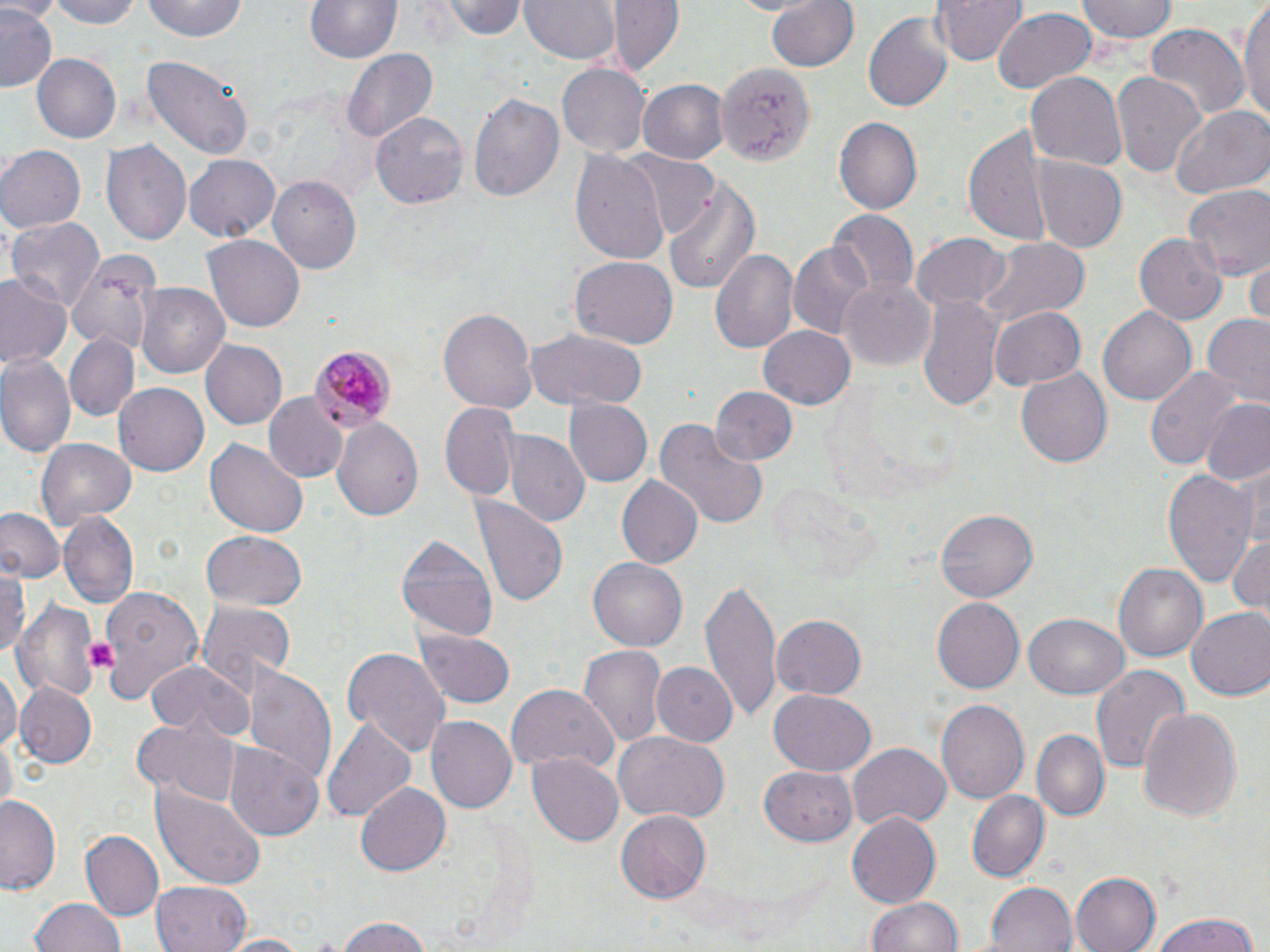
Summary:
  - Coordinate format: approximate bounding boxes as named x1/y1/x2/y2 corners in pixels
  - Platelet locations: (x1=85, y1=635, x2=118, y2=674)
  - Plasmodium malariae-infected red blood cell locations: (x1=310, y1=348, x2=396, y2=430)
  - Uninfected red blood cell locations: (x1=39, y1=0, x2=147, y2=28), (x1=140, y1=0, x2=250, y2=44), (x1=302, y1=0, x2=406, y2=65), (x1=442, y1=0, x2=527, y2=41), (x1=518, y1=0, x2=621, y2=63), (x1=608, y1=0, x2=684, y2=76), (x1=766, y1=0, x2=860, y2=75), (x1=930, y1=0, x2=1026, y2=65), (x1=1077, y1=0, x2=1178, y2=44), (x1=1239, y1=0, x2=1270, y2=123), (x1=0, y1=6, x2=60, y2=93), (x1=991, y1=6, x2=1095, y2=94), (x1=863, y1=11, x2=954, y2=112), (x1=1144, y1=26, x2=1250, y2=126), (x1=344, y1=50, x2=437, y2=144), (x1=142, y1=53, x2=253, y2=163), (x1=32, y1=55, x2=121, y2=144), (x1=715, y1=61, x2=814, y2=167), (x1=558, y1=65, x2=649, y2=155), (x1=1110, y1=69, x2=1206, y2=181), (x1=1025, y1=71, x2=1129, y2=171), (x1=640, y1=80, x2=728, y2=165), (x1=466, y1=92, x2=564, y2=204), (x1=1168, y1=104, x2=1270, y2=201), (x1=371, y1=112, x2=468, y2=211), (x1=835, y1=117, x2=922, y2=213), (x1=963, y1=123, x2=1053, y2=250), (x1=102, y1=139, x2=192, y2=245), (x1=0, y1=145, x2=84, y2=233), (x1=570, y1=151, x2=669, y2=261), (x1=625, y1=153, x2=722, y2=241), (x1=184, y1=155, x2=279, y2=241), (x1=1033, y1=157, x2=1126, y2=251), (x1=266, y1=172, x2=363, y2=274), (x1=663, y1=179, x2=759, y2=295), (x1=1185, y1=185, x2=1270, y2=281), (x1=1156, y1=202, x2=1264, y2=318), (x1=828, y1=209, x2=920, y2=297), (x1=7, y1=216, x2=103, y2=313), (x1=912, y1=233, x2=1010, y2=314), (x1=1135, y1=233, x2=1226, y2=326), (x1=202, y1=234, x2=305, y2=333), (x1=976, y1=237, x2=1092, y2=330), (x1=788, y1=243, x2=875, y2=341), (x1=64, y1=248, x2=156, y2=367), (x1=709, y1=248, x2=799, y2=355), (x1=570, y1=255, x2=677, y2=345), (x1=1247, y1=259, x2=1270, y2=325), (x1=0, y1=275, x2=69, y2=374), (x1=838, y1=278, x2=936, y2=369), (x1=135, y1=283, x2=230, y2=379), (x1=918, y1=289, x2=1001, y2=410), (x1=991, y1=304, x2=1086, y2=390), (x1=439, y1=305, x2=536, y2=417), (x1=1099, y1=306, x2=1196, y2=406), (x1=1202, y1=315, x2=1270, y2=407), (x1=757, y1=324, x2=856, y2=410), (x1=525, y1=329, x2=646, y2=410), (x1=63, y1=334, x2=140, y2=422), (x1=199, y1=339, x2=289, y2=431), (x1=0, y1=353, x2=76, y2=460), (x1=1018, y1=365, x2=1115, y2=468), (x1=1147, y1=365, x2=1242, y2=472), (x1=114, y1=384, x2=208, y2=475), (x1=709, y1=387, x2=797, y2=468), (x1=264, y1=393, x2=349, y2=484), (x1=565, y1=398, x2=652, y2=488), (x1=1199, y1=398, x2=1270, y2=485), (x1=441, y1=402, x2=519, y2=503), (x1=444, y1=414, x2=584, y2=512), (x1=331, y1=419, x2=424, y2=523), (x1=654, y1=419, x2=768, y2=531), (x1=504, y1=432, x2=590, y2=528), (x1=37, y1=439, x2=135, y2=527), (x1=204, y1=439, x2=309, y2=539), (x1=1236, y1=467, x2=1269, y2=555), (x1=1161, y1=470, x2=1260, y2=587), (x1=615, y1=475, x2=703, y2=570), (x1=471, y1=494, x2=568, y2=611), (x1=0, y1=509, x2=64, y2=585), (x1=935, y1=509, x2=1038, y2=603), (x1=60, y1=512, x2=138, y2=607), (x1=200, y1=529, x2=306, y2=608), (x1=396, y1=530, x2=499, y2=644), (x1=1226, y1=532, x2=1269, y2=616), (x1=588, y1=556, x2=687, y2=653), (x1=1115, y1=560, x2=1209, y2=663), (x1=0, y1=565, x2=28, y2=663), (x1=702, y1=580, x2=779, y2=722), (x1=97, y1=587, x2=205, y2=705), (x1=929, y1=597, x2=1024, y2=695), (x1=13, y1=598, x2=102, y2=705), (x1=195, y1=601, x2=295, y2=691), (x1=1185, y1=606, x2=1270, y2=701), (x1=1024, y1=611, x2=1129, y2=700), (x1=770, y1=615, x2=866, y2=699), (x1=415, y1=628, x2=517, y2=709), (x1=580, y1=645, x2=667, y2=749), (x1=342, y1=647, x2=449, y2=759), (x1=146, y1=661, x2=252, y2=740), (x1=650, y1=661, x2=736, y2=747), (x1=1089, y1=664, x2=1189, y2=775), (x1=241, y1=666, x2=337, y2=782), (x1=0, y1=669, x2=18, y2=757), (x1=13, y1=684, x2=97, y2=769), (x1=504, y1=685, x2=619, y2=774), (x1=767, y1=691, x2=880, y2=776), (x1=937, y1=699, x2=1031, y2=803), (x1=1136, y1=705, x2=1242, y2=822), (x1=425, y1=715, x2=516, y2=814), (x1=322, y1=716, x2=416, y2=822), (x1=132, y1=718, x2=238, y2=803), (x1=1031, y1=727, x2=1110, y2=822), (x1=613, y1=731, x2=729, y2=824), (x1=227, y1=742, x2=324, y2=843), (x1=847, y1=743, x2=950, y2=833), (x1=528, y1=753, x2=625, y2=848), (x1=759, y1=766, x2=857, y2=844), (x1=356, y1=781, x2=452, y2=876), (x1=150, y1=783, x2=266, y2=888), (x1=965, y1=789, x2=1050, y2=883), (x1=0, y1=795, x2=63, y2=896), (x1=613, y1=809, x2=710, y2=902), (x1=847, y1=813, x2=942, y2=910), (x1=80, y1=829, x2=163, y2=920), (x1=1072, y1=872, x2=1160, y2=952), (x1=982, y1=881, x2=1078, y2=952), (x1=152, y1=882, x2=250, y2=952), (x1=866, y1=895, x2=962, y2=952), (x1=30, y1=899, x2=128, y2=952), (x1=1149, y1=912, x2=1263, y2=952), (x1=335, y1=917, x2=437, y2=952), (x1=217, y1=934, x2=314, y2=952)
  - Slide-level diagnosis: Plasmodium malariae
  - Magnification: 1000x
  - Stain: May-Grünwald-Giemsa
  - Modality: optical microscopy
  - Field of view: one of a larger specimen
  - Image size: 1270×952 pixels
  - Preparation: thin blood smear